Assess the morphology of the red blood cells.
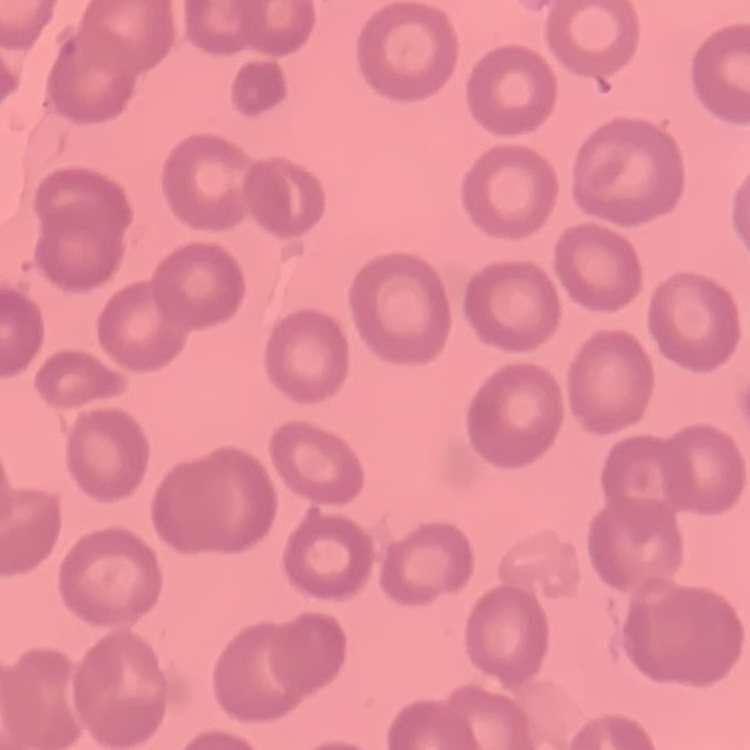

They show no rouleaux formation.

Summary:
  - Stain: Field's or Giemsa
  - Preparation: thin blood film
  - Image type: one tile cut from a larger photomicrograph